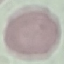 Result: no malaria parasites seen. Automatically extracted cell patch, resized to 64 × 64 pixels. Giemsa-stained preparation. Thin smear of blood. Acquired by smartphone through the microscope eyepiece.